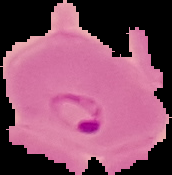
malaria status = parasitized
image size = 172×175 pixels
preparation = thin blood smear
image type = cell region segmented out of the field of view; surrounding area masked to black